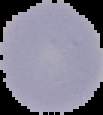
From a thin blood smear. Image is 103×115 pixels. Malaria status: uninfected. The area outside the segmented cell region is set to black.